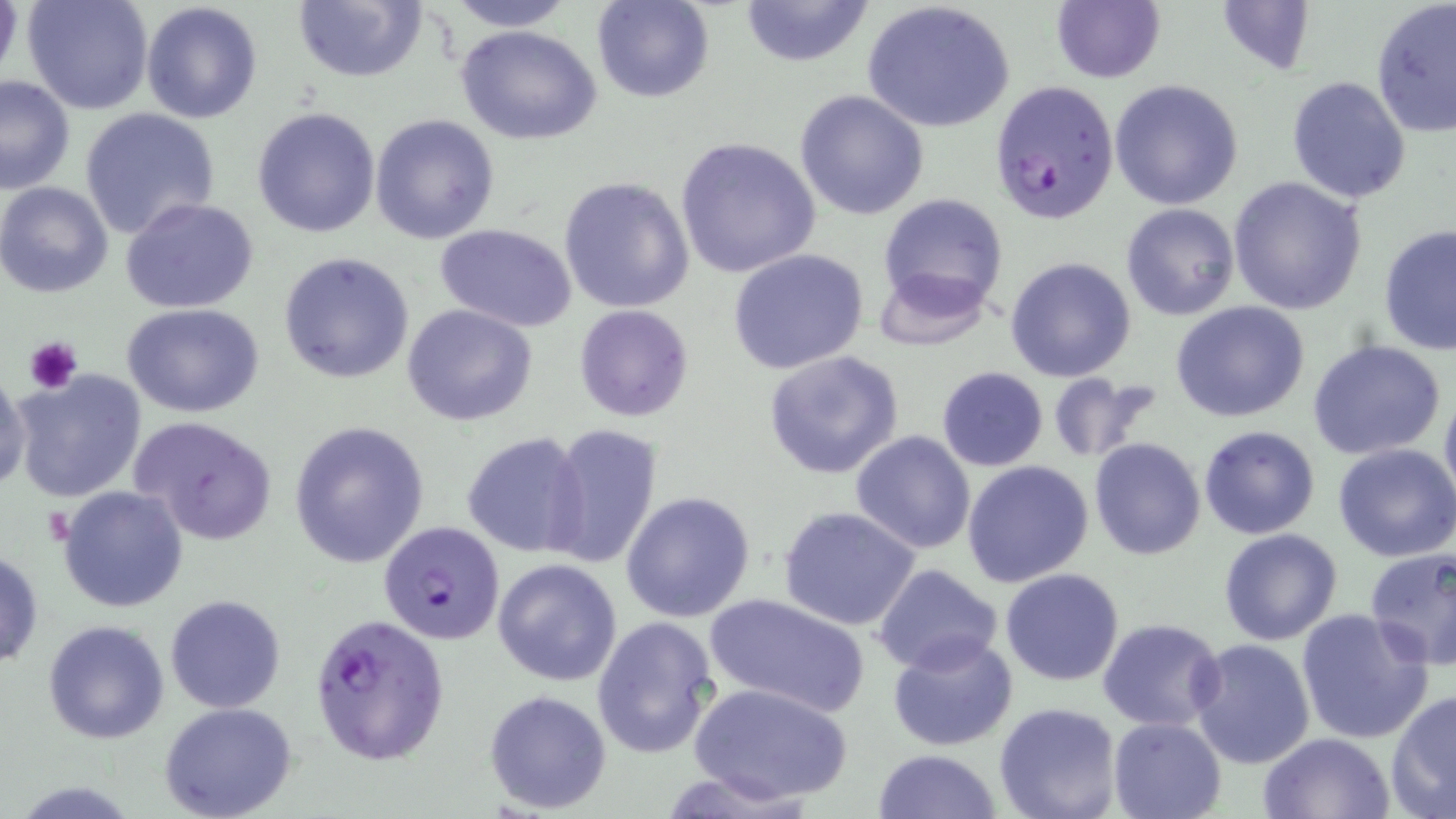

Approximate bounding boxes as (x1,y1)-(x2,y2) corner pairs in pixels. Platelet locations: (24,336)-(83,395). Plasmodium falciparum-infected red blood cell locations: (988,79)-(1120,223), (377,520)-(506,644), (309,612)-(450,765). Uninfected red blood cell locations: (0,0)-(24,94), (23,0)-(155,115), (442,0)-(577,31), (592,0)-(714,103), (737,0)-(876,69), (1215,0)-(1319,77), (140,1)-(263,125), (292,1)-(427,84), (862,1)-(1016,135), (1370,1)-(1456,139), (1049,2)-(1166,83), (454,23)-(602,145), (0,75)-(75,194), (1286,76)-(1412,204), (1109,79)-(1244,211), (794,88)-(930,221), (252,106)-(381,238), (79,107)-(221,239), (370,114)-(499,245), (674,136)-(821,279), (558,176)-(695,313), (1227,177)-(1368,315), (0,181)-(117,299), (878,192)-(1009,316), (120,198)-(260,315), (1119,204)-(1239,320), (434,224)-(578,332), (1378,225)-(1456,355), (728,249)-(870,375), (278,252)-(415,384), (1005,256)-(1136,382), (873,266)-(992,350), (1171,301)-(1312,422), (122,302)-(267,419), (401,303)-(539,426), (574,304)-(694,422), (1307,339)-(1448,460), (762,349)-(905,481), (936,366)-(1049,472), (10,368)-(149,505), (0,369)-(29,490), (1045,374)-(1161,463), (1439,384)-(1456,517), (129,415)-(279,545), (288,421)-(430,568), (541,423)-(663,570), (1197,425)-(1321,539), (462,431)-(591,558), (850,431)-(978,555), (1088,437)-(1206,561), (1332,444)-(1456,563), (962,460)-(1095,588), (57,484)-(188,613), (621,490)-(755,623), (778,506)-(921,631), (1218,528)-(1342,644), (1364,546)-(1456,669), (0,547)-(45,671), (492,558)-(621,686), (873,563)-(1004,675), (1000,568)-(1125,685), (703,594)-(871,718), (165,595)-(287,713), (1295,608)-(1433,747), (592,615)-(719,762), (41,618)-(170,744), (1097,618)-(1226,733), (887,633)-(1020,752), (1190,638)-(1316,768), (689,681)-(853,805), (483,688)-(612,814), (1387,690)-(1456,818), (158,701)-(299,819), (994,703)-(1124,819), (1107,716)-(1227,819), (1258,732)-(1393,818), (874,747)-(1002,818). Slide-level diagnosis: Plasmodium falciparum. Light microscopy. Image is 1456×819 pixels. Single field of view. Thin blood film. Captured at 1000x magnification. May-Grünwald-Giemsa-stained preparation.